Classify this cell by malaria status.
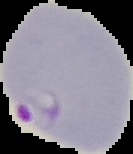
It is parasitized.

{
  "image_size": "133×154 pixels",
  "image_type": "segmented cell region with the area outside set to black",
  "preparation": "thin blood film"
}